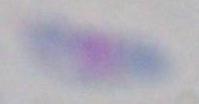

{
  "modality": "micrograph",
  "identification": "Toxoplasma gondii",
  "magnification": "1000x"
}